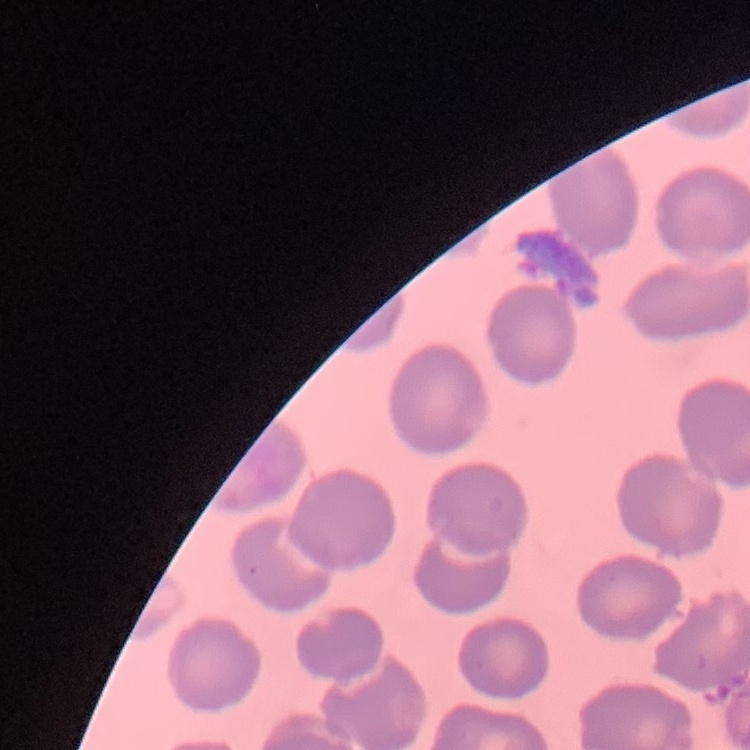

erythrocyte morphology = no rouleaux formation
image type = one tile cut from a larger photomicrograph
stain = Field's or Giemsa
preparation = thin blood film